Report the malaria status of this cell.
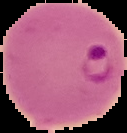
It is parasitized.

Segmented cell region on a black background. Image is 127×133 pixels. From a thin blood smear.